Outline each Plasmodium ovale-infected red blood cell.
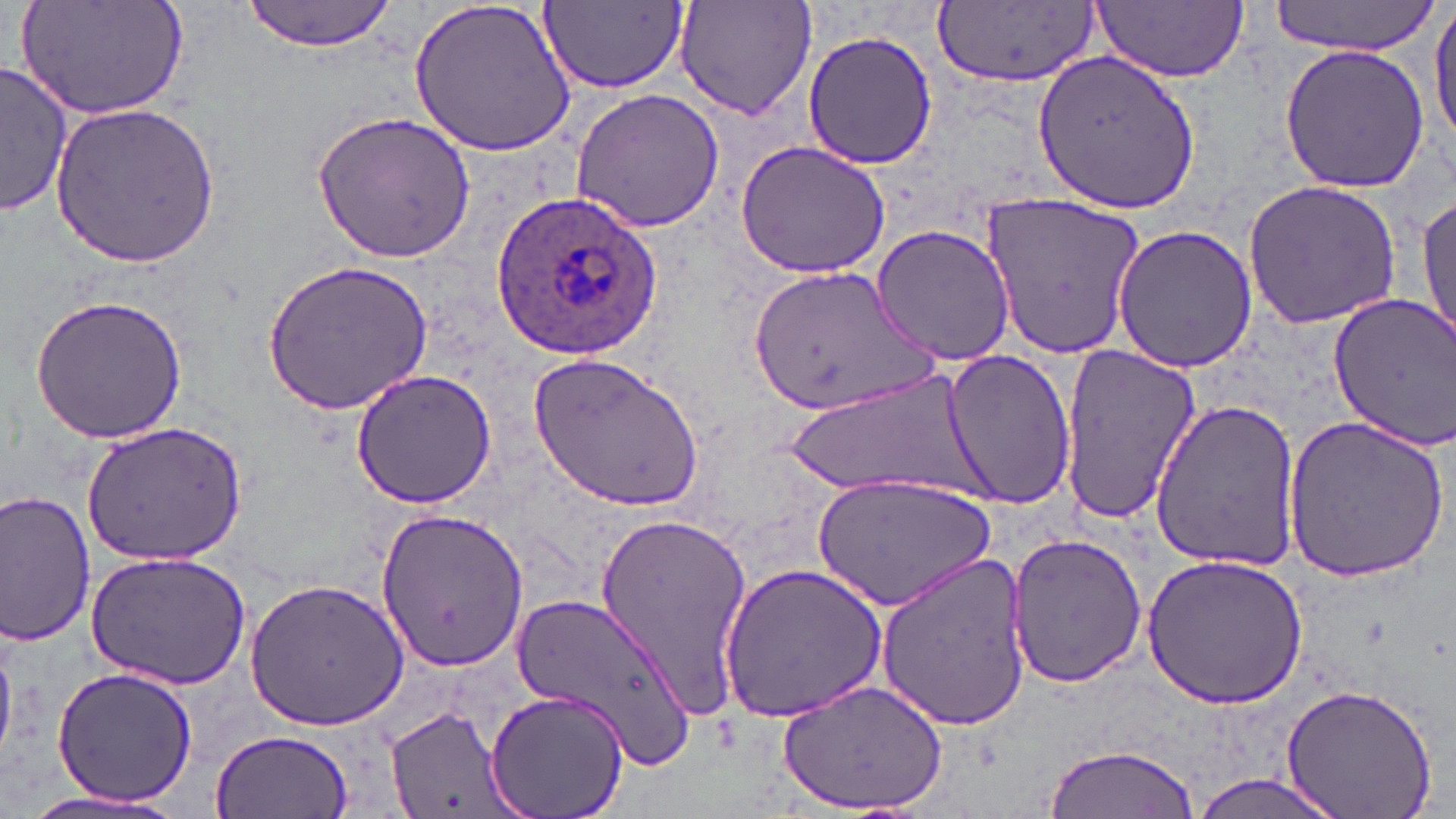

Approximate bounding boxes as named x1/y1/x2/y2 corners in pixels.
Plasmodium ovale-infected red blood cells: (x1=492, y1=187, x2=663, y2=362).

Uninfected red blood cell locations: (x1=15, y1=0, x2=191, y2=121), (x1=242, y1=0, x2=399, y2=53), (x1=406, y1=0, x2=578, y2=158), (x1=675, y1=0, x2=817, y2=122), (x1=1269, y1=0, x2=1443, y2=54), (x1=539, y1=1, x2=688, y2=92), (x1=936, y1=1, x2=1099, y2=84), (x1=1091, y1=1, x2=1247, y2=83), (x1=1429, y1=2, x2=1456, y2=159), (x1=802, y1=25, x2=937, y2=173), (x1=1278, y1=43, x2=1431, y2=193), (x1=1031, y1=49, x2=1202, y2=215), (x1=1, y1=63, x2=73, y2=217), (x1=570, y1=88, x2=726, y2=234), (x1=48, y1=101, x2=226, y2=268), (x1=310, y1=109, x2=479, y2=264), (x1=735, y1=140, x2=891, y2=277), (x1=1243, y1=178, x2=1402, y2=331), (x1=981, y1=190, x2=1148, y2=360), (x1=1416, y1=192, x2=1455, y2=349), (x1=871, y1=222, x2=1015, y2=365), (x1=1110, y1=224, x2=1258, y2=373), (x1=264, y1=260, x2=433, y2=415), (x1=742, y1=263, x2=936, y2=418), (x1=29, y1=292, x2=188, y2=443), (x1=1326, y1=293, x2=1456, y2=450), (x1=1058, y1=344, x2=1203, y2=529), (x1=942, y1=351, x2=1076, y2=510), (x1=530, y1=352, x2=703, y2=514), (x1=349, y1=368, x2=499, y2=510), (x1=772, y1=373, x2=1002, y2=498), (x1=1150, y1=396, x2=1303, y2=572), (x1=1281, y1=416, x2=1449, y2=583), (x1=83, y1=423, x2=246, y2=563), (x1=813, y1=473, x2=997, y2=612), (x1=0, y1=484, x2=98, y2=649), (x1=377, y1=505, x2=528, y2=672), (x1=592, y1=509, x2=753, y2=716), (x1=1007, y1=531, x2=1147, y2=689), (x1=81, y1=549, x2=252, y2=691), (x1=874, y1=551, x2=1032, y2=733), (x1=1141, y1=551, x2=1310, y2=709), (x1=720, y1=560, x2=886, y2=724), (x1=245, y1=577, x2=410, y2=732), (x1=510, y1=589, x2=693, y2=765), (x1=49, y1=665, x2=197, y2=806), (x1=776, y1=677, x2=949, y2=814), (x1=1279, y1=683, x2=1438, y2=819), (x1=483, y1=689, x2=631, y2=819), (x1=384, y1=702, x2=523, y2=819), (x1=210, y1=728, x2=353, y2=819), (x1=1042, y1=745, x2=1202, y2=818), (x1=1188, y1=771, x2=1348, y2=819), (x1=8, y1=790, x2=191, y2=816). Slide-level diagnosis: Plasmodium ovale. 1000x magnification. Thin blood smear. May-Grünwald-Giemsa-stained preparation. Image is 1456×819 pixels. Light microscopy. Single field of view.